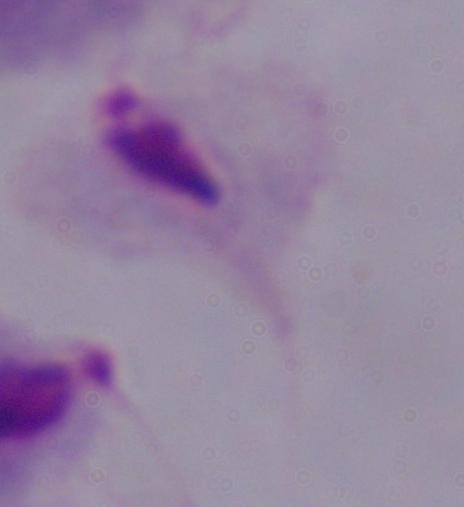

Summary:
  - Identification: trichomonad
  - Modality: photomicrograph
  - Magnification: 1000x